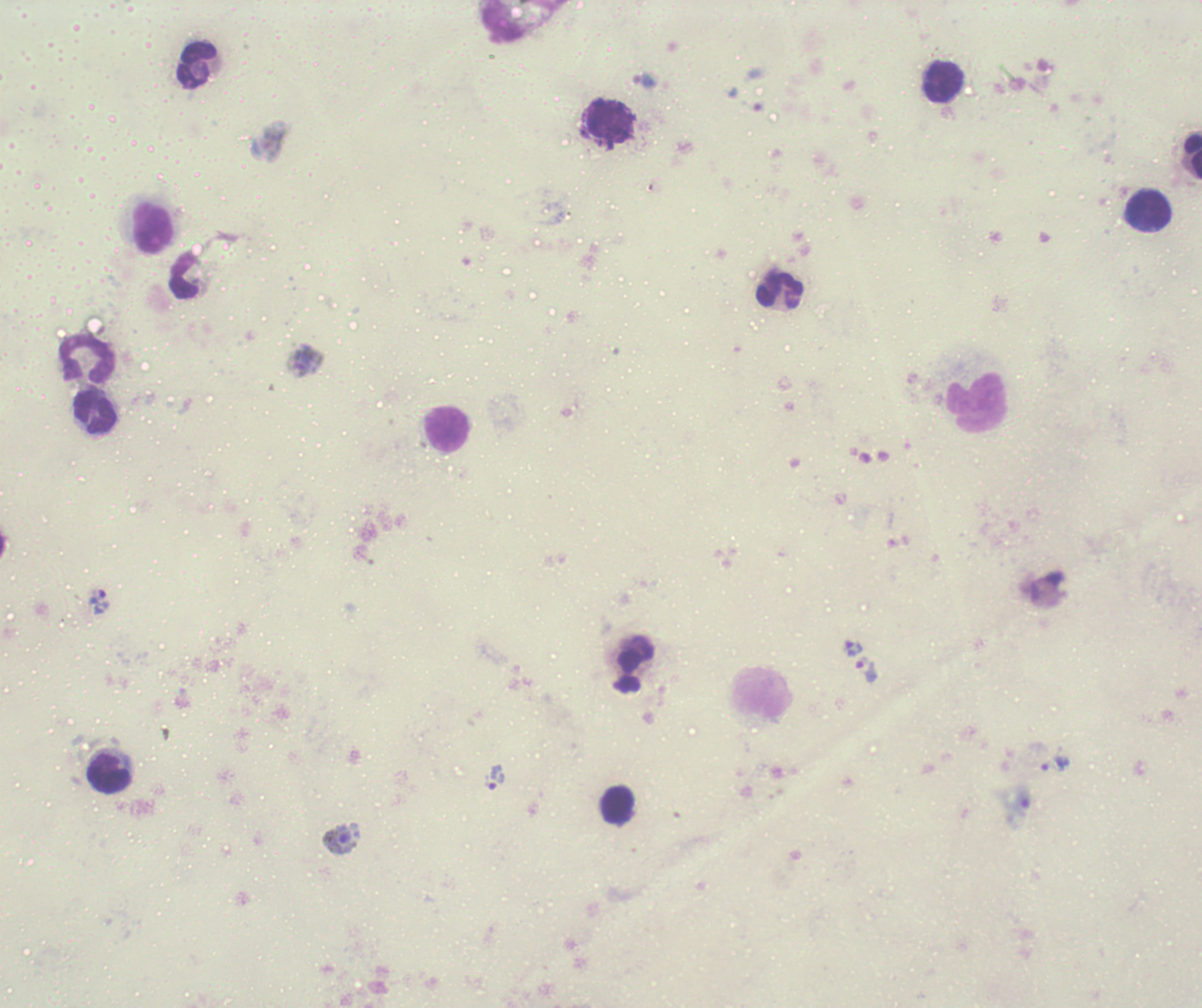

Approximate centers as (x, y) in pixels. Trophozoite locations: (644, 81), (99, 599), (854, 648), (866, 669), (1056, 764), (496, 778). Leukocyte locations: (196, 66), (944, 82), (609, 120), (1193, 156), (1149, 209), (153, 228), (184, 275), (780, 291), (88, 359), (976, 403), (95, 410), (446, 430), (109, 773), (619, 805). Gametocyte locations: (304, 361), (341, 839). Life-cycle stages observed: trophozoite, gametocyte. 100x magnification. Coloration quality: bad. Background quality: unsatisfactory. Romanowsky stain. Previously used in a real diagnosis. One field from this slide. Result: malaria parasites detected. Thick blood smear. Image is 1202×1008 pixels.